Describe the morphology of the red blood cells.
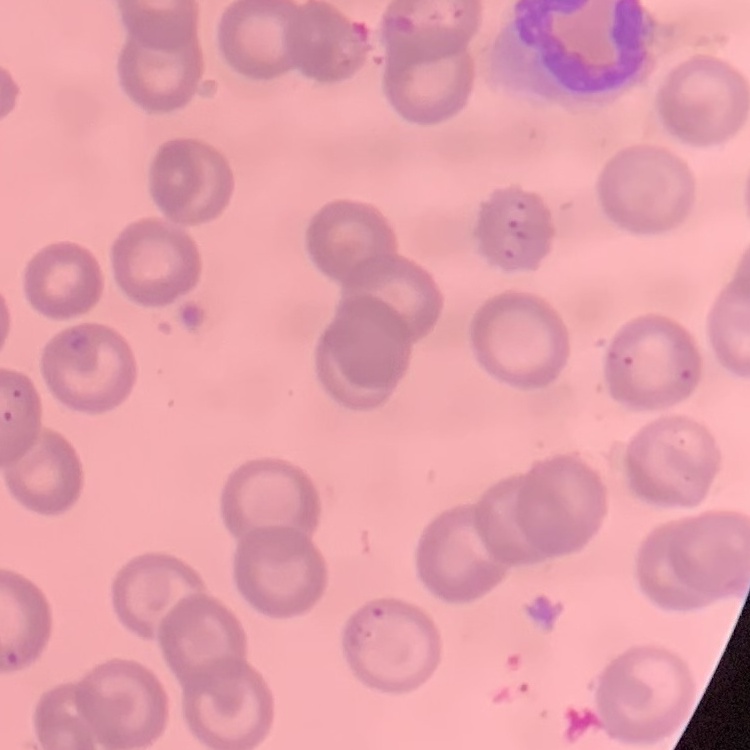
No rouleaux formation.

Square crop of a larger photomicrograph. Field's or Giemsa stain. Thin blood film.